Classify this cell by malaria status.
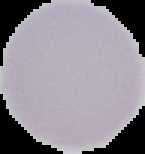

It is uninfected.

Segmented cell region on a black background. From a thin blood film. Image is 145×154 pixels.